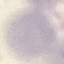
Summary:
  - Malaria status: uninfected
  - Image type: cell patch, automatically extracted from a larger field of view and resized to 64 × 64 pixels
  - Preparation: thin blood film
  - Capture: smartphone through the microscope eyepiece
  - Stain: Giemsa